Describe the morphology of the red blood cells.
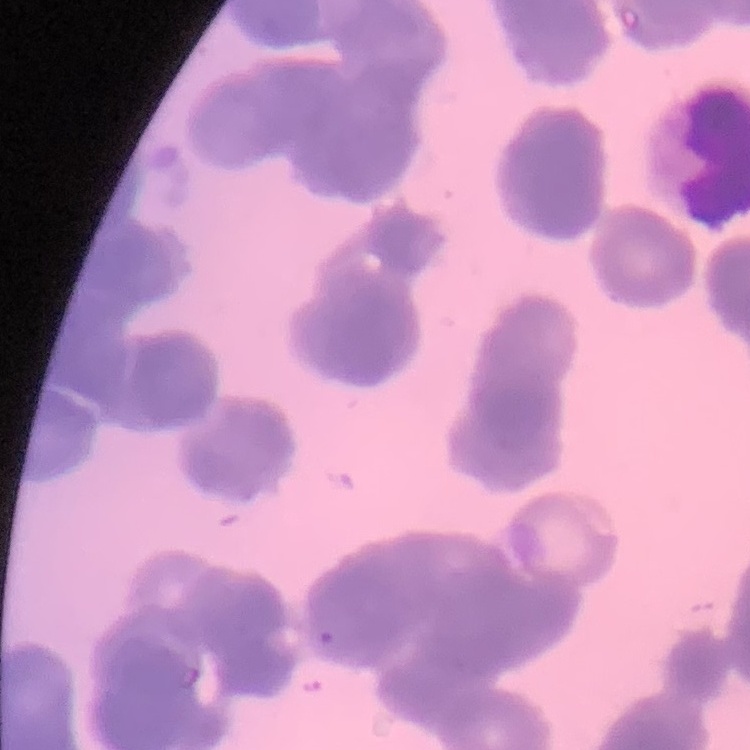
They show rouleaux formation.

Stained with either Field's or Giemsa. Square crop of a larger photomicrograph. Thin blood film.